Report the malaria status of this cell.
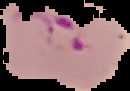

Parasitized.

Summary:
  - Image type: segmented cell region with the area outside set to black
  - Preparation: thin blood smear
  - Image size: 130×91 pixels